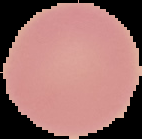

From a thin blood smear. The area outside the segmented cell region is set to black. Malaria status: uninfected. Image is 142×139 pixels.